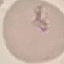

Summary:
  - Result: malaria parasites identified
  - Image type: automatically extracted cell patch, resized to 64 × 64 pixels
  - Capture: smartphone through the microscope eyepiece
  - Stain: Giemsa
  - Preparation: thin blood film